Locate every blood parasite and identify its species.
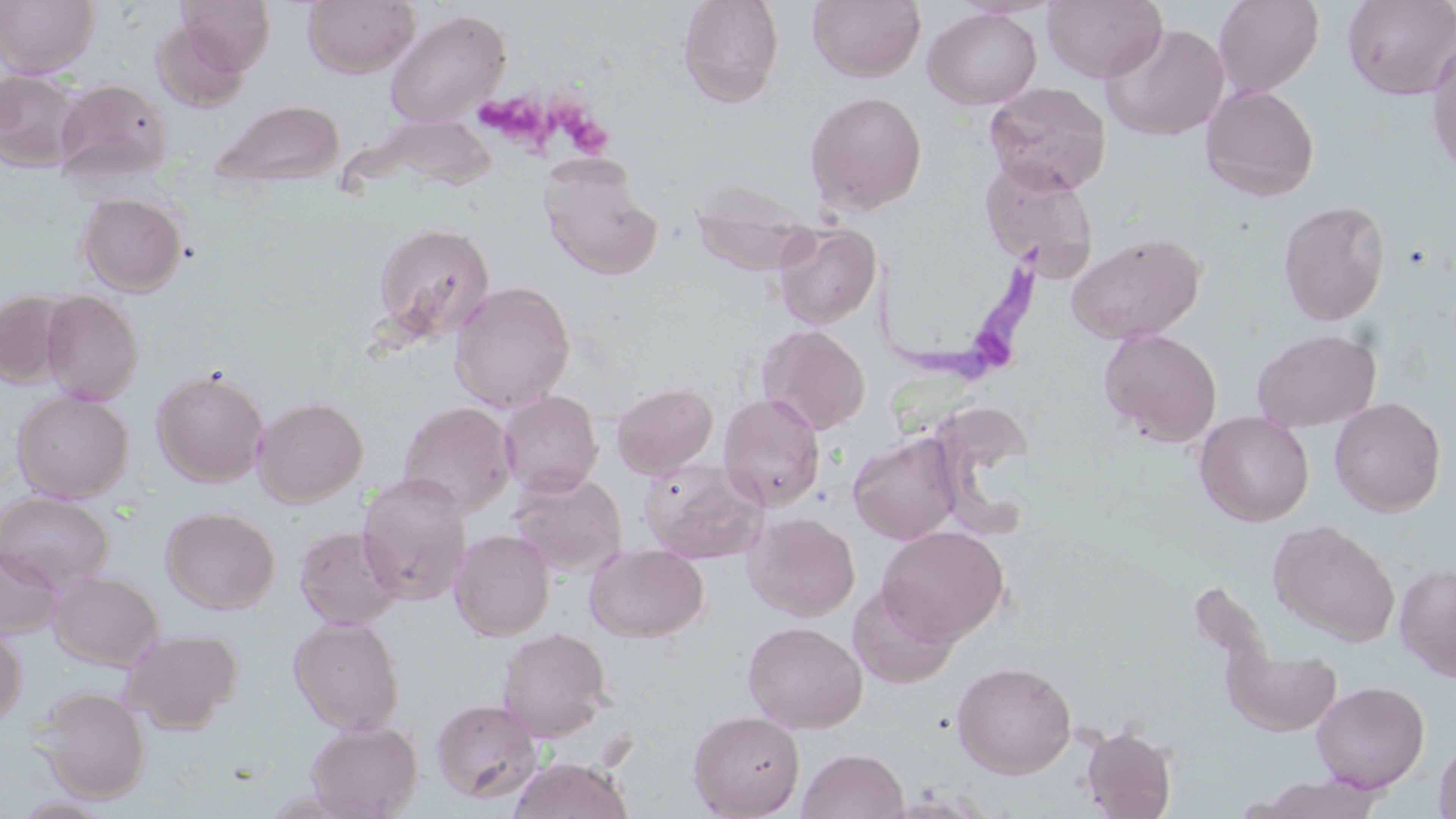
Approximate bounding boxes as [x1, y1, x2, y2] in pixels.
Trypanosoma brucei: [873, 234, 1060, 383].
No Plasmodium falciparum, Plasmodium ovale, Plasmodium malariae, Plasmodium vivax, or Babesia divergens observed.

Uninfected red blood cell locations: [0, 0, 99, 78], [177, 0, 276, 74], [303, 0, 419, 77], [677, 0, 785, 107], [807, 0, 926, 83], [1043, 0, 1167, 82], [1213, 0, 1324, 97], [1342, 0, 1456, 100], [922, 7, 1042, 110], [385, 9, 511, 127], [151, 19, 251, 114], [1102, 22, 1231, 141], [1426, 36, 1456, 177], [0, 70, 83, 171], [53, 78, 172, 183], [983, 81, 1111, 195], [1200, 84, 1320, 201], [805, 91, 927, 215], [213, 98, 346, 190], [979, 158, 1100, 278], [542, 166, 662, 280], [690, 177, 818, 274], [76, 192, 188, 296], [1277, 200, 1390, 325], [370, 222, 495, 344], [772, 222, 881, 329], [1066, 232, 1205, 344], [448, 280, 576, 412], [0, 290, 74, 387], [41, 290, 143, 404], [757, 324, 870, 435], [1099, 328, 1222, 447], [1252, 328, 1381, 431], [152, 367, 269, 487], [611, 382, 719, 479], [12, 390, 132, 502], [499, 390, 603, 497], [718, 392, 826, 510], [253, 396, 368, 506], [1329, 397, 1446, 516], [398, 401, 517, 516], [1194, 411, 1314, 526], [934, 416, 1036, 536], [847, 431, 964, 545], [640, 458, 769, 564], [509, 471, 627, 575], [356, 474, 473, 605], [0, 492, 113, 592], [160, 506, 280, 614], [744, 511, 860, 621], [1268, 520, 1400, 647], [294, 525, 404, 629], [876, 525, 1009, 644], [449, 529, 555, 640], [585, 544, 708, 642], [0, 545, 62, 639], [1394, 562, 1456, 682], [48, 570, 163, 671], [848, 580, 960, 689], [288, 616, 405, 734], [742, 620, 867, 734], [0, 624, 27, 727], [496, 627, 614, 742], [121, 628, 243, 734], [1222, 646, 1342, 735], [952, 661, 1077, 779], [1311, 680, 1429, 793], [36, 686, 151, 803], [431, 697, 543, 803], [687, 710, 805, 819], [305, 719, 422, 819], [1081, 723, 1177, 819], [1433, 737, 1456, 819], [797, 748, 909, 819], [508, 756, 635, 818], [1250, 775, 1387, 818]. Platelet locations: [470, 85, 614, 163]. Slide-level diagnosis: Trypanosoma brucei. Thin blood smear. 1000x magnification. May-Grünwald-Giemsa stain. One field of a larger specimen. Image is 1456×819 pixels. Optical microscopy.